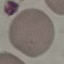
{
  "result": "no malaria parasites seen",
  "stain": "Giemsa",
  "image_type": "cell patch, automatically extracted from a larger field of view and resized to 64 × 64 pixels",
  "capture": "smartphone camera at the microscope eyepiece",
  "preparation": "thin smear"
}